Locate and identify every blood parasite.
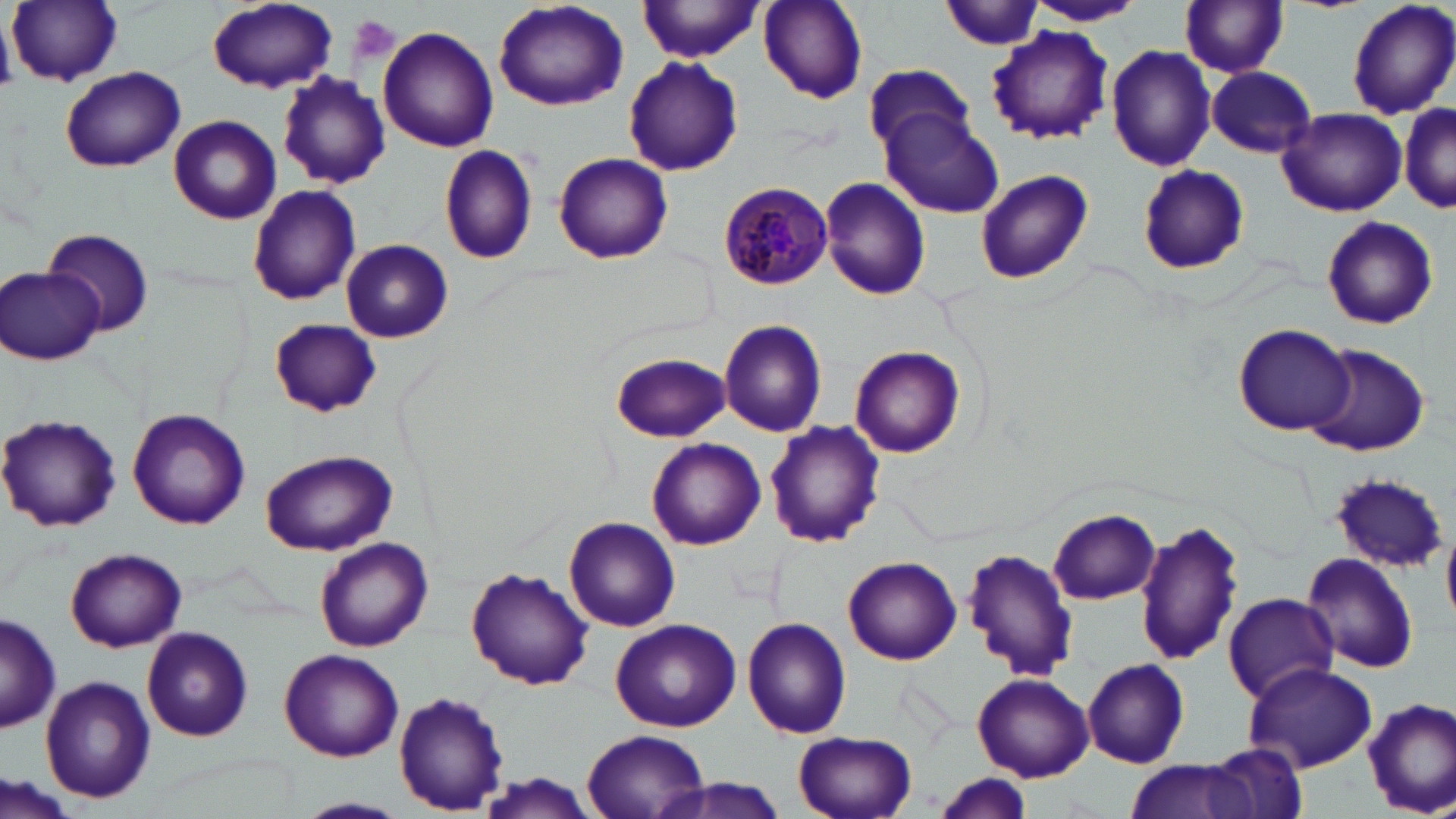
Approximate bounding boxes as (x1, y1, x2, y2) in pixels.
Plasmodium malariae-infected red blood cells: (717, 182, 833, 290).
No Plasmodium falciparum, Plasmodium ovale, Plasmodium vivax, Babesia divergens, or Trypanosoma brucei observed.

slide-level diagnosis = Plasmodium malariae
modality = optical microscopy
uninfected red blood cell locations = approximate bounding boxes as (x1, y1, x2, y2) in pixels: (8, 0, 122, 86), (937, 0, 1045, 51), (1348, 0, 1456, 120), (757, 1, 867, 104), (1021, 1, 1146, 26), (206, 2, 338, 94), (492, 2, 628, 111), (639, 2, 765, 62), (1179, 2, 1288, 78), (987, 25, 1114, 145), (378, 26, 499, 151), (1106, 44, 1216, 173), (623, 58, 743, 176), (863, 62, 974, 156), (60, 66, 185, 172), (1208, 66, 1317, 157), (279, 73, 391, 187), (1399, 105, 1456, 214), (1277, 107, 1407, 217), (881, 110, 1006, 218), (170, 115, 281, 222), (439, 142, 538, 264), (554, 152, 673, 264), (1136, 165, 1249, 276), (975, 170, 1093, 285), (818, 176, 932, 301), (246, 184, 361, 304), (1319, 215, 1439, 329), (45, 227, 154, 336), (341, 239, 452, 344), (0, 267, 102, 365), (269, 318, 380, 416), (718, 319, 828, 437), (1233, 322, 1355, 437), (1303, 344, 1431, 456), (850, 345, 966, 458), (610, 351, 732, 441), (127, 408, 252, 530), (0, 413, 122, 534), (765, 421, 886, 548), (646, 437, 766, 550), (259, 449, 398, 556), (1328, 473, 1447, 573), (1047, 509, 1160, 604), (564, 517, 682, 632), (1136, 520, 1244, 668), (312, 536, 433, 652), (64, 547, 185, 651), (964, 547, 1080, 683), (1301, 552, 1420, 675), (843, 555, 961, 665), (466, 569, 593, 691), (1222, 592, 1338, 704), (0, 615, 61, 733), (743, 617, 852, 738), (609, 618, 742, 732), (142, 627, 254, 741), (277, 648, 405, 762), (1082, 658, 1190, 768), (1244, 664, 1378, 772), (973, 673, 1094, 781), (41, 676, 155, 804), (392, 692, 510, 813), (1363, 698, 1456, 817), (581, 729, 710, 818), (793, 731, 917, 818), (1202, 740, 1311, 818), (1121, 759, 1267, 819), (469, 772, 604, 818), (3, 774, 80, 819), (933, 775, 1034, 818), (654, 776, 790, 819), (296, 796, 410, 818)
field of view = one of a larger specimen
platelet locations = approximate bounding boxes as (x1, y1, x2, y2) in pixels: (350, 16, 400, 64)
stain = May-Grünwald-Giemsa
magnification = 1000x
image size = 1456×819 pixels
preparation = thin blood film